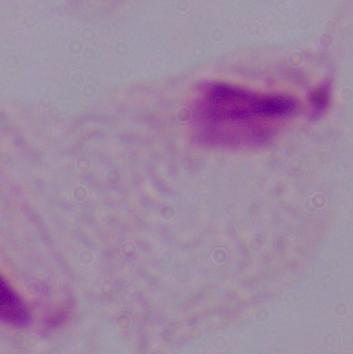
Summary:
  - Magnification: 1000x
  - Modality: micrograph
  - Identification: trichomonad